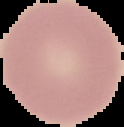

image type = segmented cell region on a black background
image size = 124×127 pixels
preparation = thin blood film
malaria status = uninfected